Assess this cell for malaria.
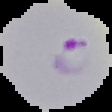

Parasitized.

image_type: segmented cell region with the area outside set to black
preparation: thin blood smear
image_size: 112×112 pixels